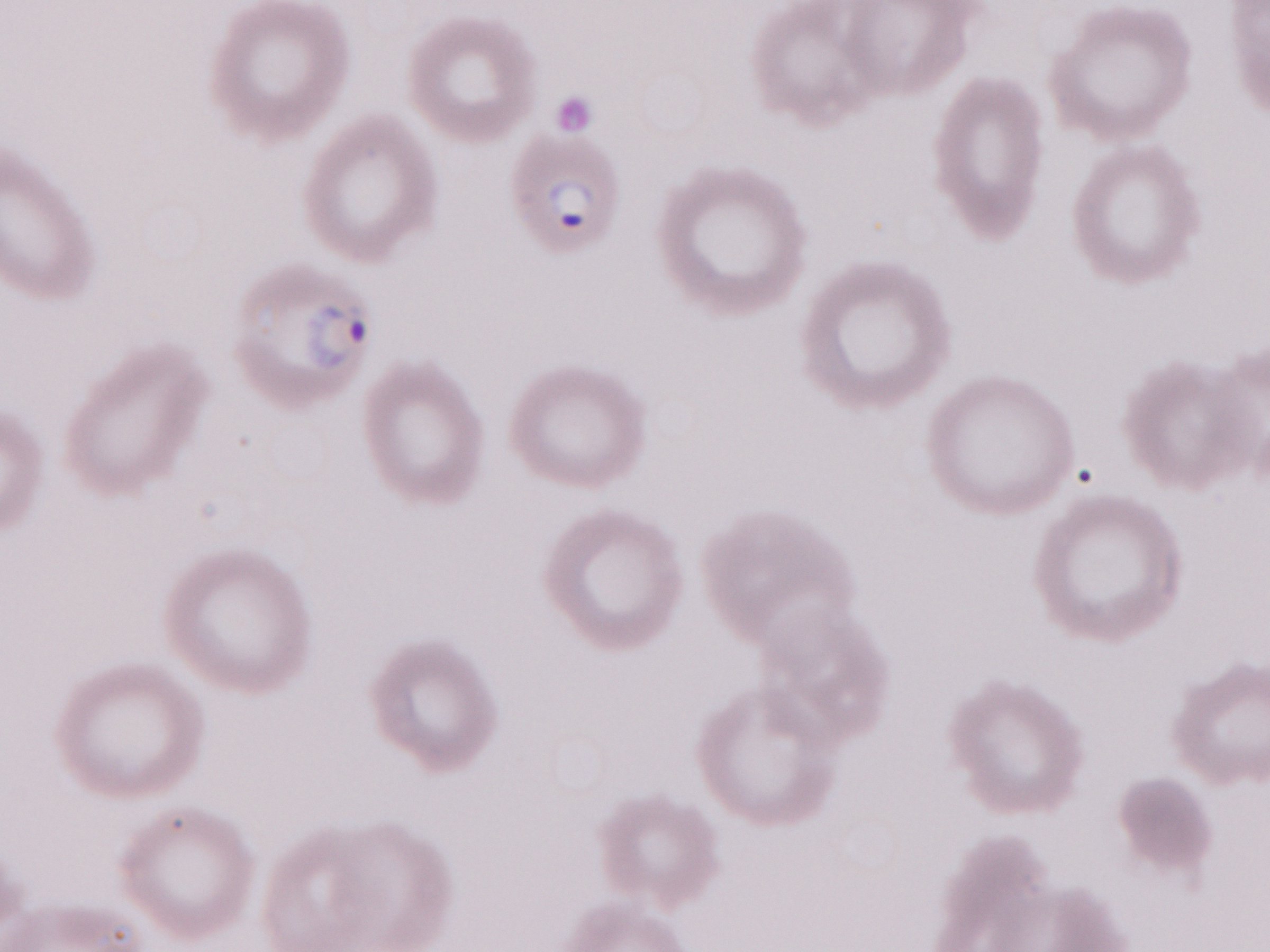 Magnification: 1,000x. May-Grünwald-Giemsa stain. One field of this slide. Olympus BX43 microscope, Olympus DP73 camera. Patient-level malaria diagnosis: positive. Image is 1270×952 pixels. Thin peripheral-blood smear.